Comment on the morphology of the red blood cells.
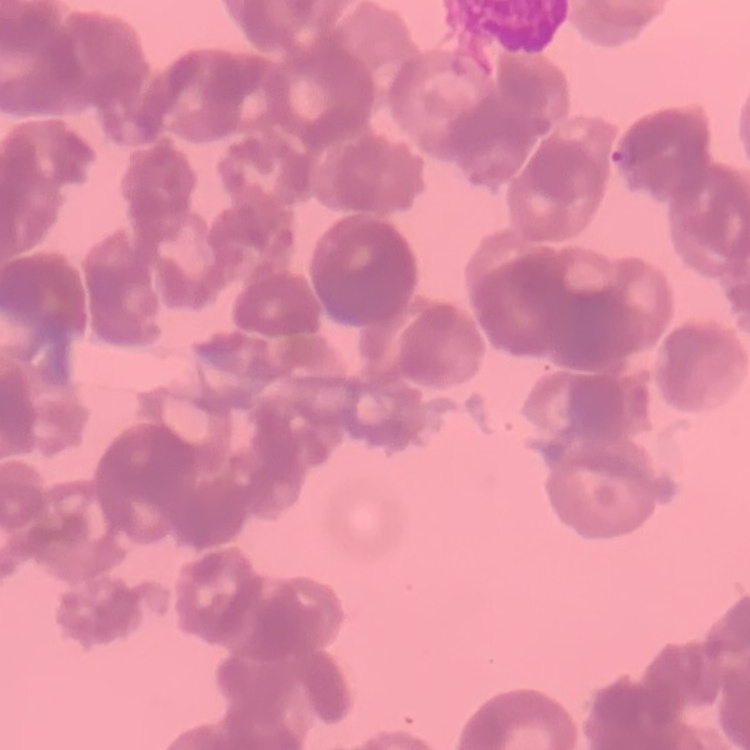
Rouleaux formation.

Thin blood film. One tile cut from a larger photomicrograph. Field's or Giemsa stain.